Point out each Plasmodium parasite.
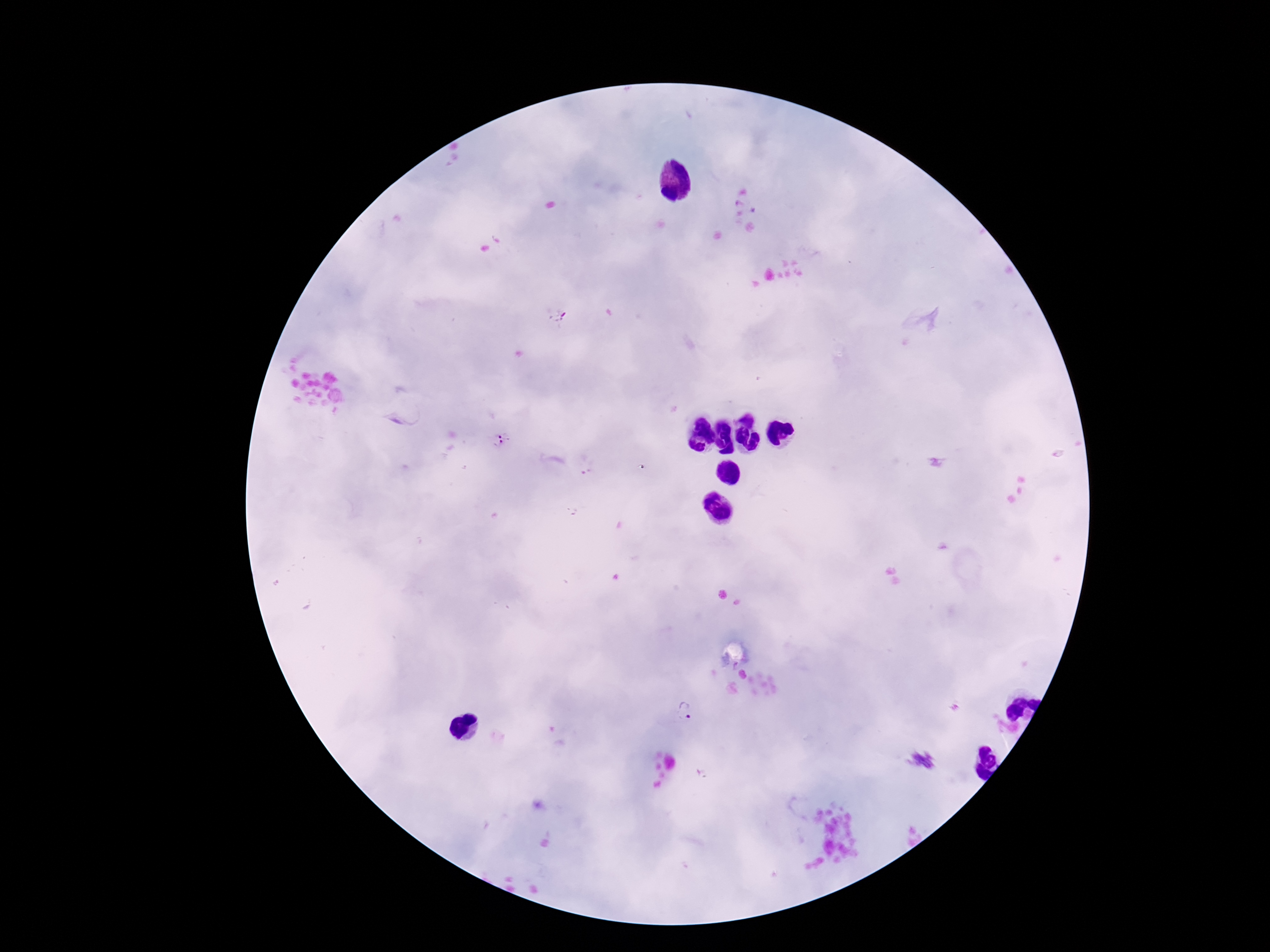

Approximate centers as (x, y) in pixels.
Plasmodium parasites: (558, 315), (501, 440), (686, 712), (924, 759).

Summary:
  - Image size: 1270×952 pixels
  - Preparation: thick blood smear
  - Capture: smartphone camera through the microscope eyepiece
  - Patient malaria status: positive
  - Magnification: 100x
  - Stain: Giemsa
  - Field of view: single